Describe the morphology of the red blood cells.
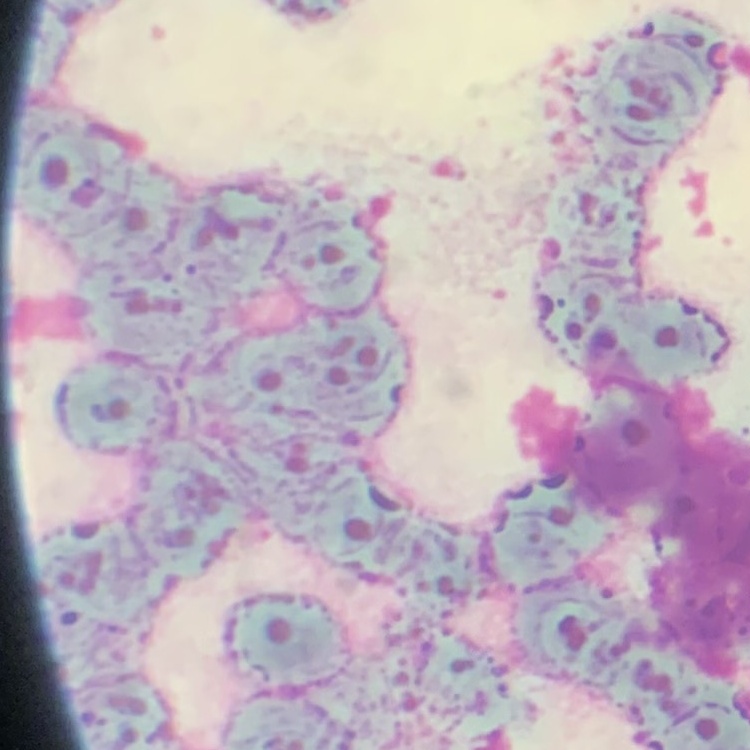
They show rouleaux formation.

Summary:
  - Image type: square crop of a larger photomicrograph
  - Preparation: thin blood film
  - Stain: Field's or Giemsa